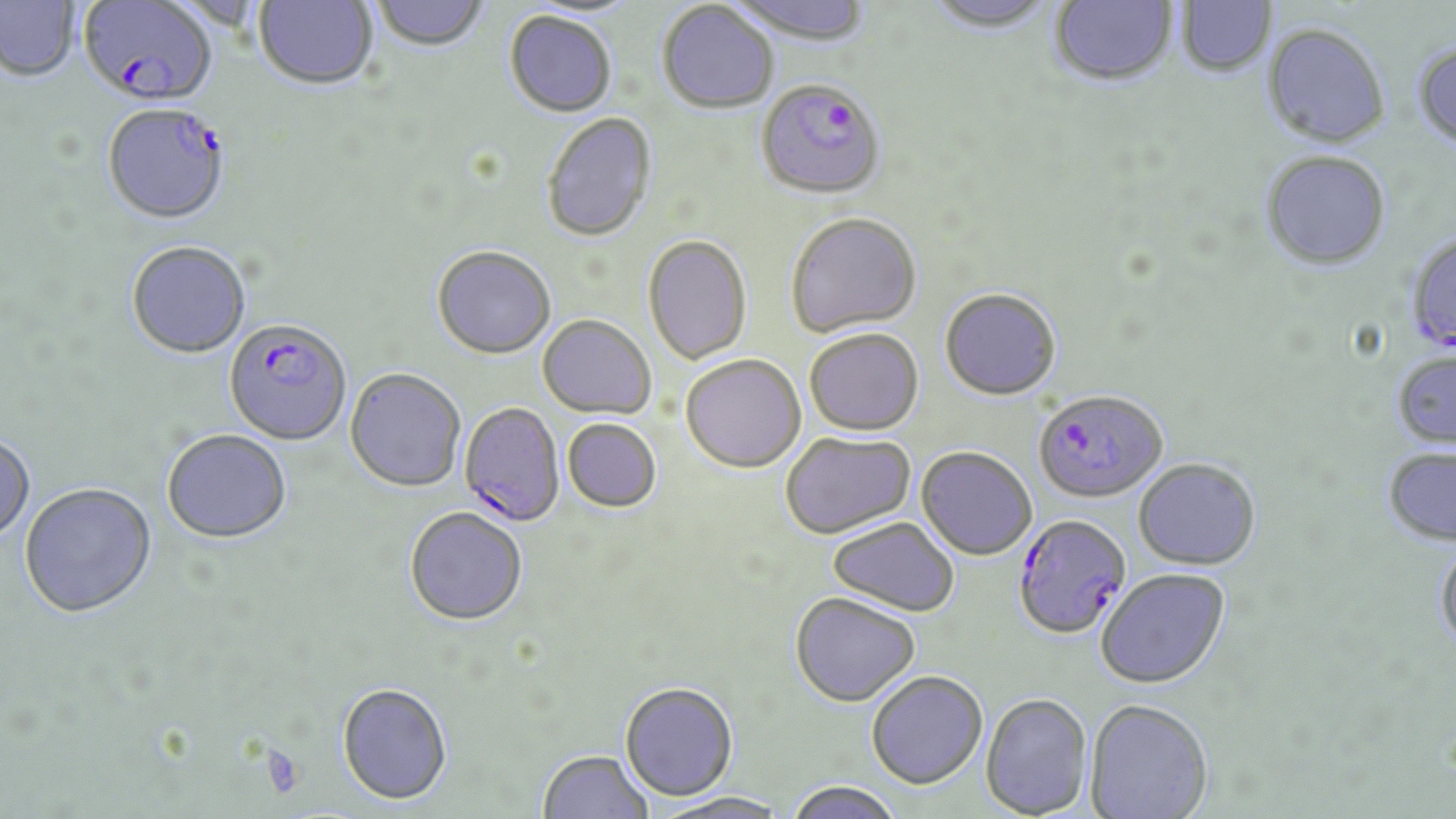 Approximate bounding boxes as [x1, y1, x2, y2] in pixels. Plasmodium falciparum-infected red blood cell locations: [79, 0, 217, 106], [756, 79, 886, 200], [103, 103, 230, 224], [1405, 233, 1456, 354], [224, 320, 352, 446], [1034, 390, 1167, 503], [459, 403, 565, 528], [1013, 515, 1131, 640]. Uninfected red blood cell locations: [372, 0, 489, 53], [729, 0, 873, 45], [1049, 0, 1177, 88], [1175, 0, 1276, 78], [0, 1, 81, 82], [254, 1, 378, 91], [925, 1, 1058, 36], [657, 2, 779, 114], [504, 12, 617, 119], [1261, 24, 1390, 149], [1412, 40, 1456, 153], [541, 114, 657, 243], [1260, 151, 1392, 271], [786, 213, 922, 338], [643, 235, 752, 364], [126, 241, 251, 359], [432, 247, 556, 360], [939, 288, 1061, 400], [537, 315, 656, 419], [804, 328, 924, 436], [1392, 351, 1456, 449], [680, 354, 806, 473], [344, 369, 466, 493], [562, 418, 662, 512], [161, 429, 291, 545], [780, 431, 915, 539], [0, 433, 36, 544], [1382, 446, 1456, 547], [916, 447, 1037, 560], [1133, 458, 1261, 570], [19, 483, 156, 619], [405, 507, 528, 627], [828, 516, 960, 616], [1434, 539, 1456, 657], [1096, 568, 1230, 688], [789, 592, 920, 706], [866, 670, 987, 789], [620, 681, 738, 800], [337, 683, 453, 805], [980, 692, 1093, 818], [1084, 697, 1213, 819], [537, 749, 654, 819], [783, 780, 905, 819], [653, 791, 792, 819]. Platelet locations: [260, 745, 307, 799]. Slide-level diagnosis: Plasmodium falciparum. Light microscopy. May-Grünwald-Giemsa stain. Thin blood smear. Image is 1456×819 pixels. 1000x magnification. Single field of view.